Identify the blood parasite species.
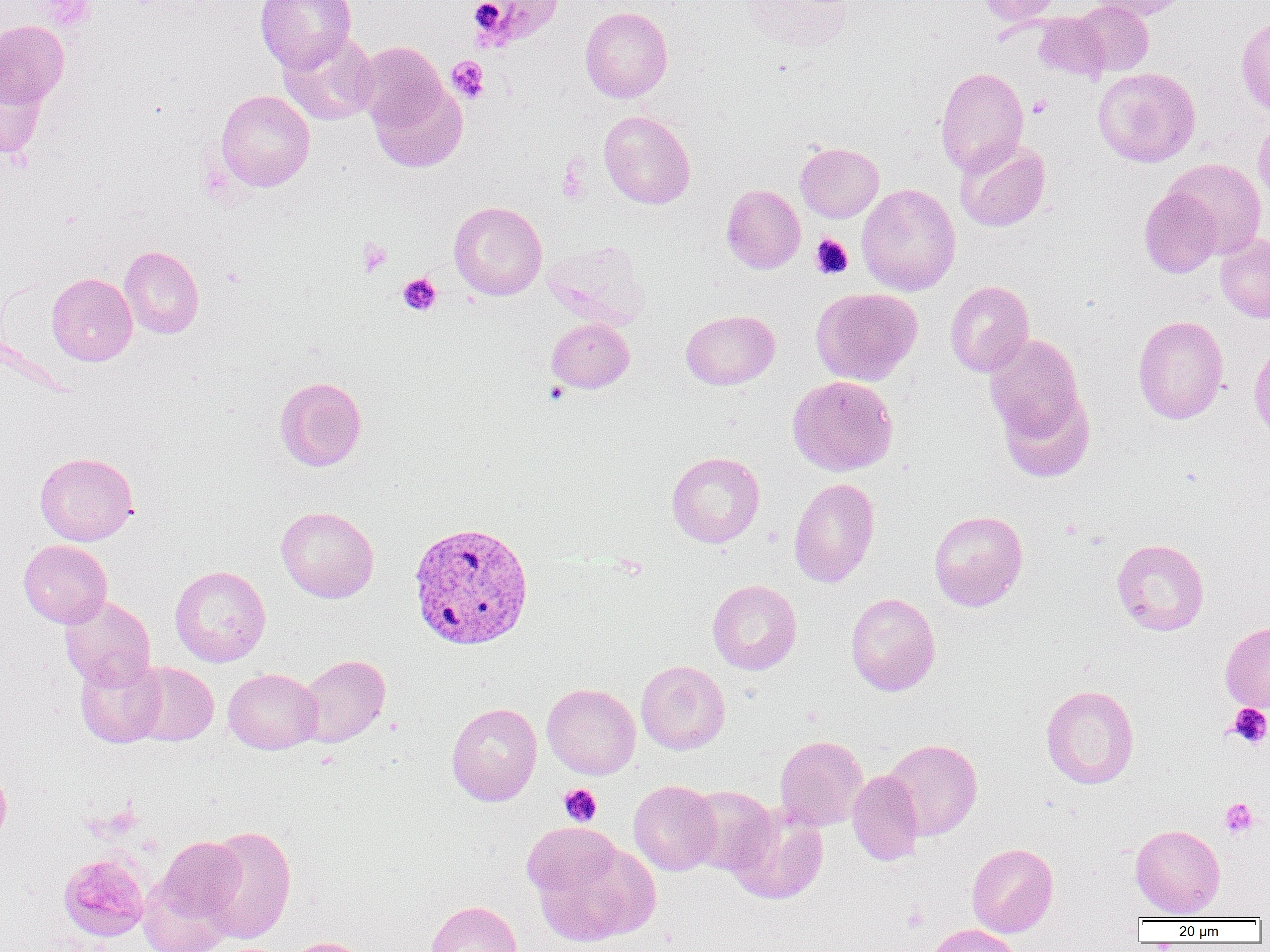

Plasmodium vivax.

preparation: thin blood smear
plasmodium_vivax_infected_red_blood_cell_locations: 'approximate bounding boxes as named x1/y1/x2/y2 corners in pixels: (x1=407, y1=521, x2=535, y2=650)'
uninfected_red_blood_cell_locations: 'approximate bounding boxes as named x1/y1/x2/y2 corners in pixels: (x1=255, y1=0, x2=356, y2=72), (x1=467, y1=0, x2=564, y2=50), (x1=742, y1=0, x2=853, y2=53), (x1=978, y1=0, x2=1061, y2=26), (x1=1073, y1=0, x2=1154, y2=77), (x1=1089, y1=0, x2=1190, y2=21), (x1=580, y1=7, x2=673, y2=102), (x1=1033, y1=12, x2=1110, y2=83), (x1=1236, y1=16, x2=1270, y2=118), (x1=0, y1=20, x2=69, y2=107), (x1=278, y1=30, x2=379, y2=125), (x1=355, y1=41, x2=448, y2=133), (x1=0, y1=63, x2=47, y2=158), (x1=935, y1=67, x2=1029, y2=176), (x1=1093, y1=67, x2=1201, y2=167), (x1=369, y1=79, x2=467, y2=173), (x1=215, y1=90, x2=315, y2=192), (x1=598, y1=110, x2=696, y2=209), (x1=1253, y1=115, x2=1270, y2=208), (x1=955, y1=139, x2=1051, y2=232), (x1=795, y1=142, x2=883, y2=222), (x1=1164, y1=158, x2=1267, y2=259), (x1=857, y1=183, x2=961, y2=296), (x1=721, y1=184, x2=805, y2=274), (x1=1139, y1=187, x2=1222, y2=278), (x1=449, y1=201, x2=547, y2=301), (x1=1216, y1=233, x2=1270, y2=323), (x1=543, y1=242, x2=649, y2=329), (x1=119, y1=246, x2=204, y2=338), (x1=46, y1=273, x2=137, y2=366), (x1=945, y1=280, x2=1034, y2=377), (x1=811, y1=287, x2=923, y2=386), (x1=680, y1=310, x2=780, y2=390), (x1=1132, y1=315, x2=1229, y2=424), (x1=546, y1=318, x2=634, y2=393), (x1=984, y1=334, x2=1086, y2=443), (x1=1248, y1=341, x2=1270, y2=444), (x1=787, y1=375, x2=898, y2=476), (x1=275, y1=376, x2=367, y2=471), (x1=997, y1=385, x2=1096, y2=483), (x1=34, y1=451, x2=138, y2=546), (x1=666, y1=451, x2=764, y2=548), (x1=788, y1=477, x2=880, y2=588), (x1=276, y1=506, x2=378, y2=603), (x1=928, y1=510, x2=1028, y2=611), (x1=1111, y1=538, x2=1210, y2=635), (x1=18, y1=539, x2=112, y2=627), (x1=170, y1=565, x2=271, y2=667), (x1=707, y1=580, x2=802, y2=675), (x1=845, y1=593, x2=941, y2=696), (x1=59, y1=595, x2=156, y2=690), (x1=1220, y1=621, x2=1270, y2=713), (x1=297, y1=654, x2=390, y2=747), (x1=75, y1=657, x2=166, y2=748), (x1=636, y1=660, x2=730, y2=755), (x1=127, y1=662, x2=219, y2=746), (x1=223, y1=668, x2=323, y2=754), (x1=542, y1=683, x2=641, y2=779), (x1=1041, y1=684, x2=1139, y2=789), (x1=447, y1=697, x2=639, y2=791), (x1=446, y1=702, x2=542, y2=806), (x1=775, y1=735, x2=869, y2=831), (x1=882, y1=738, x2=983, y2=840), (x1=0, y1=765, x2=11, y2=846), (x1=847, y1=770, x2=924, y2=866), (x1=629, y1=780, x2=721, y2=875), (x1=686, y1=786, x2=776, y2=875), (x1=725, y1=804, x2=828, y2=904), (x1=1130, y1=824, x2=1225, y2=918), (x1=197, y1=825, x2=297, y2=943), (x1=526, y1=831, x2=661, y2=947), (x1=152, y1=836, x2=247, y2=927), (x1=966, y1=843, x2=1059, y2=937), (x1=58, y1=852, x2=149, y2=942), (x1=136, y1=868, x2=236, y2=952), (x1=426, y1=900, x2=522, y2=952), (x1=923, y1=923, x2=1023, y2=952), (x1=280, y1=936, x2=372, y2=952)'
field_of_view: one of a larger specimen
magnification: 1000x
platelet_locations: 'approximate bounding boxes as named x1/y1/x2/y2 corners in pixels: (x1=37, y1=0, x2=95, y2=30), (x1=446, y1=56, x2=489, y2=102), (x1=1027, y1=95, x2=1052, y2=117), (x1=557, y1=162, x2=590, y2=205), (x1=810, y1=234, x2=853, y2=279), (x1=357, y1=238, x2=392, y2=277), (x1=397, y1=272, x2=442, y2=316), (x1=1226, y1=703, x2=1270, y2=749), (x1=559, y1=784, x2=602, y2=826), (x1=1219, y1=798, x2=1258, y2=838), (x1=902, y1=903, x2=927, y2=931)'
modality: optical microscopy
image_size: 1270×952 pixels